Comment on the morphology of the erythrocytes.
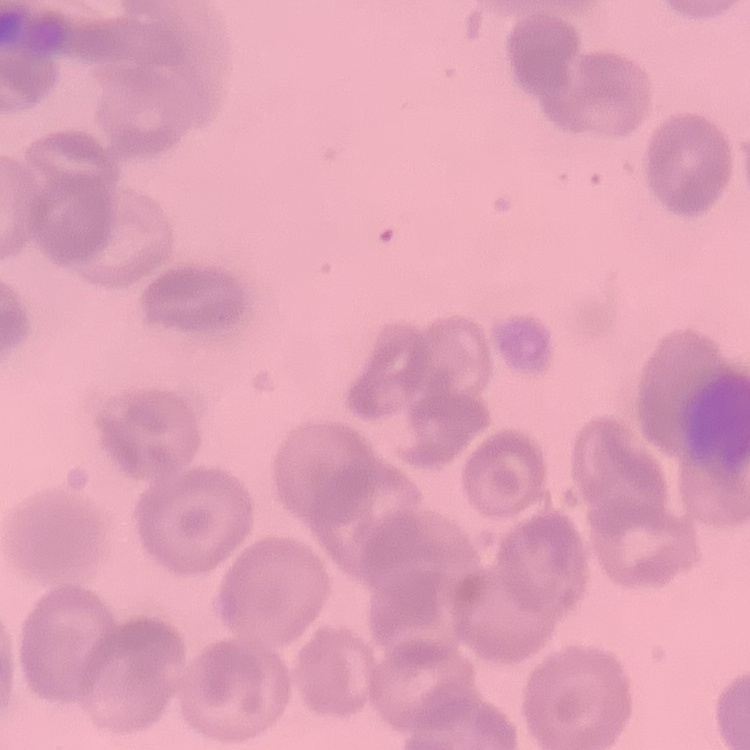
They show no rouleaux formation.

Summary:
  - Image type: one tile cut from a larger photomicrograph
  - Preparation: thin blood smear
  - Stain: Field's or Giemsa